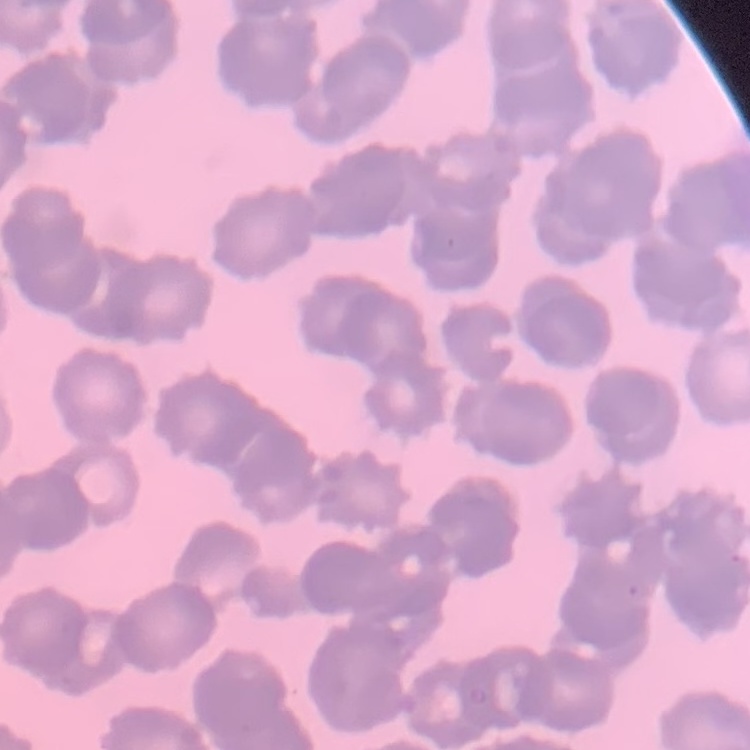 The erythrocytes show rouleaux formation. Thin peripheral smear. Stained with either Field's or Giemsa. Square crop of a larger photomicrograph.